Assess this cell for malaria.
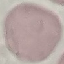
It is uninfected.

Cell patch, automatically extracted from a larger field of view and resized to 64 × 64 pixels. Thin blood smear. Acquired by smartphone through the microscope eyepiece. Giemsa-stained preparation.